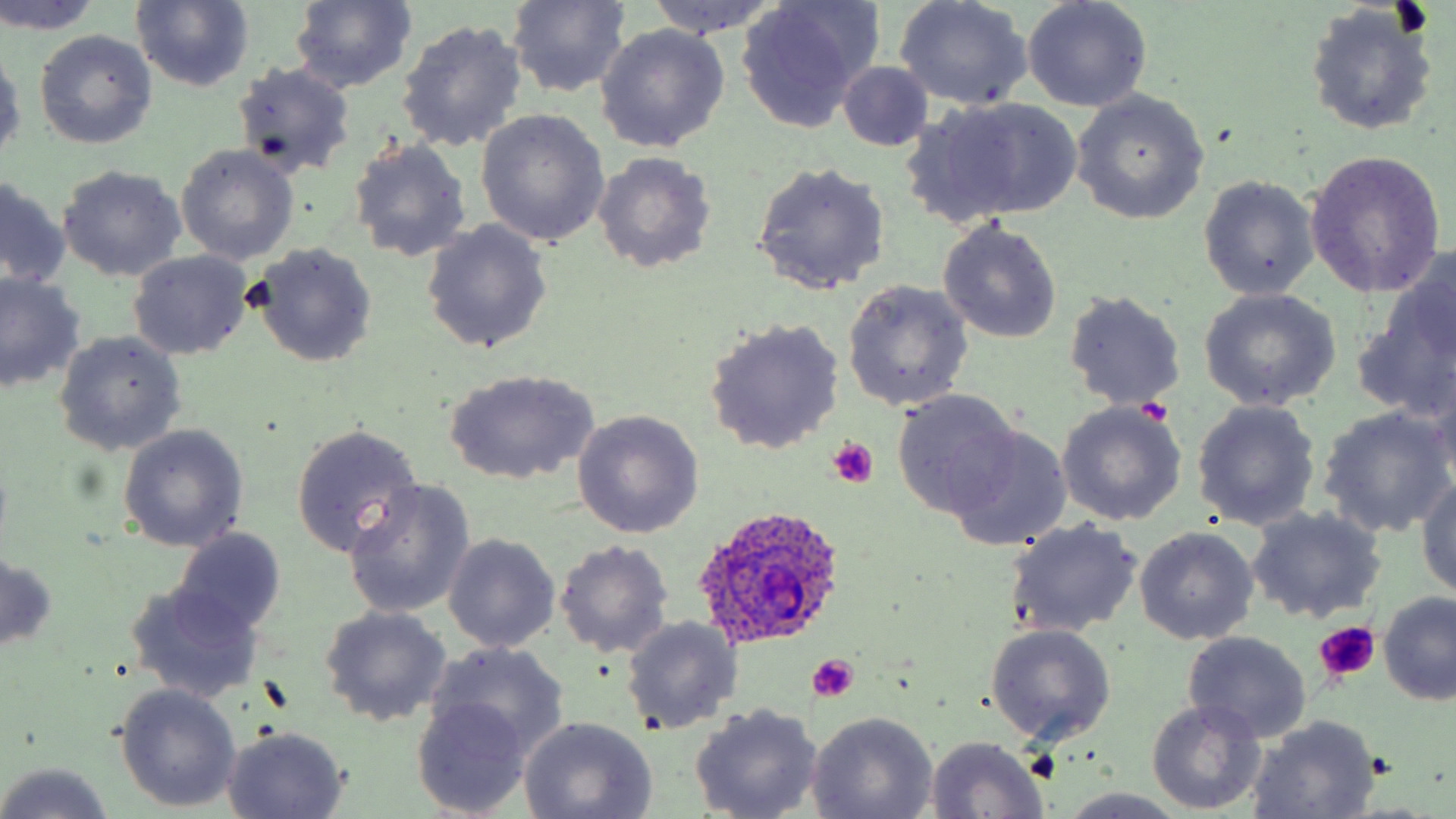

Summary:
  - Coordinate format: approximate bounding boxes as (x1, y1, x2, y2) in pixels
  - Plasmodium ovale-infected red blood cell locations: (693, 508, 850, 651)
  - Platelet locations: (824, 437, 880, 488), (1313, 623, 1379, 685), (805, 655, 859, 702)
  - Uninfected red blood cell locations: (131, 0, 255, 92), (642, 0, 783, 39), (894, 0, 1030, 111), (289, 1, 417, 92), (507, 1, 630, 95), (1021, 1, 1151, 113), (0, 2, 101, 34), (732, 2, 881, 130), (1304, 2, 1441, 137), (396, 20, 528, 156), (596, 25, 730, 153), (35, 30, 157, 149), (0, 43, 24, 166), (837, 61, 934, 151), (232, 62, 357, 179), (1072, 91, 1210, 224), (923, 97, 1083, 223), (475, 110, 611, 248), (347, 139, 472, 261), (175, 144, 299, 266), (1303, 150, 1447, 298), (593, 152, 717, 274), (751, 163, 890, 295), (56, 165, 188, 282), (0, 177, 72, 289), (1199, 177, 1320, 301), (938, 220, 1063, 343), (420, 222, 551, 355), (250, 245, 378, 368), (128, 251, 252, 362), (1375, 252, 1456, 381), (0, 273, 85, 394), (841, 280, 973, 412), (1198, 288, 1341, 410), (1064, 291, 1185, 410), (1355, 299, 1455, 421), (703, 319, 845, 454), (53, 331, 186, 456), (444, 369, 598, 484), (891, 391, 1022, 518), (1192, 400, 1321, 530), (1056, 402, 1187, 527), (1318, 405, 1454, 538), (573, 409, 703, 538), (290, 423, 423, 556), (118, 425, 247, 551), (943, 425, 1073, 551), (1415, 473, 1456, 600), (342, 482, 475, 618), (1246, 507, 1388, 623), (1005, 519, 1142, 638), (171, 526, 286, 637), (1133, 526, 1259, 644), (443, 534, 560, 654), (555, 540, 673, 659), (1, 551, 58, 653), (123, 582, 267, 705), (1378, 594, 1456, 706), (318, 606, 452, 726), (621, 617, 741, 735), (985, 625, 1115, 745), (1183, 632, 1311, 742), (428, 642, 571, 759), (114, 683, 240, 811), (413, 698, 533, 817), (1145, 701, 1265, 815), (689, 705, 823, 819), (807, 712, 938, 819), (517, 716, 659, 818), (1246, 716, 1381, 819), (221, 724, 349, 817), (924, 736, 1049, 817), (0, 763, 115, 819), (1060, 790, 1193, 818)
  - Slide-level diagnosis: Plasmodium ovale
  - Magnification: 1000x
  - Modality: light microscopy
  - Preparation: thin blood smear
  - Stain: May-Grünwald-Giemsa
  - Field of view: one of a larger specimen
  - Image size: 1456×819 pixels